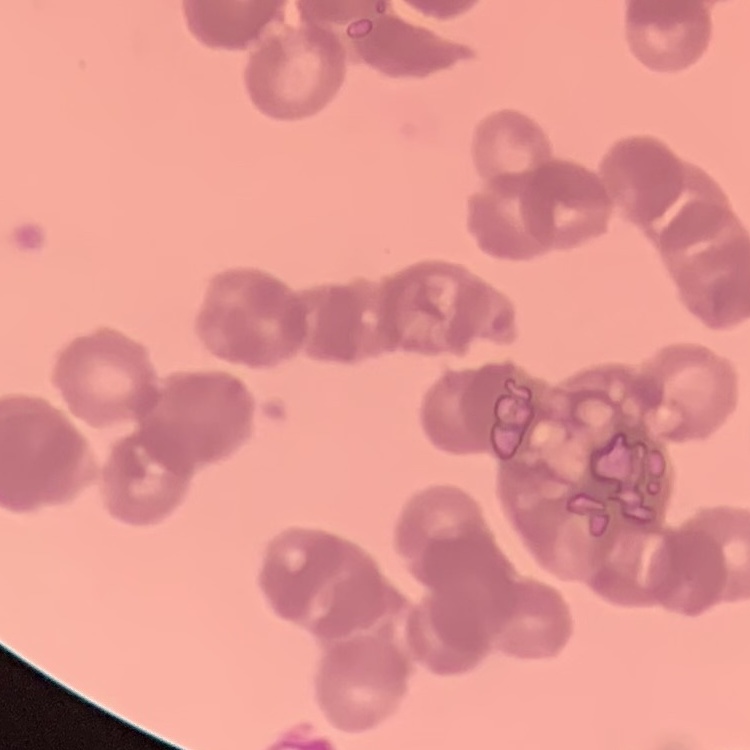
The red blood cells show rouleaux formation. Thin blood smear. Square crop of a larger photomicrograph. Field's or Giemsa stain.